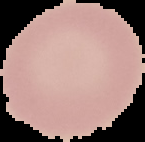
image_size: 145×142 pixels
malaria_status: uninfected
preparation: thin blood film
image_type: cell region segmented out of the field of view; surrounding area masked to black